Identify the cell.
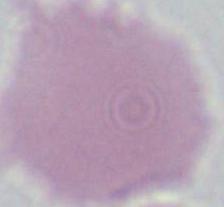
This is an erythrocyte.

Summary:
  - Modality: micrograph
  - Magnification: 1000x